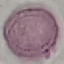

Malaria status: uninfected. Giemsa stain. Cell patch, automatically extracted from a larger field of view and resized to 64 × 64 pixels. Thin smear of blood. Acquired by smartphone through the microscope eyepiece.